Outline platelets.
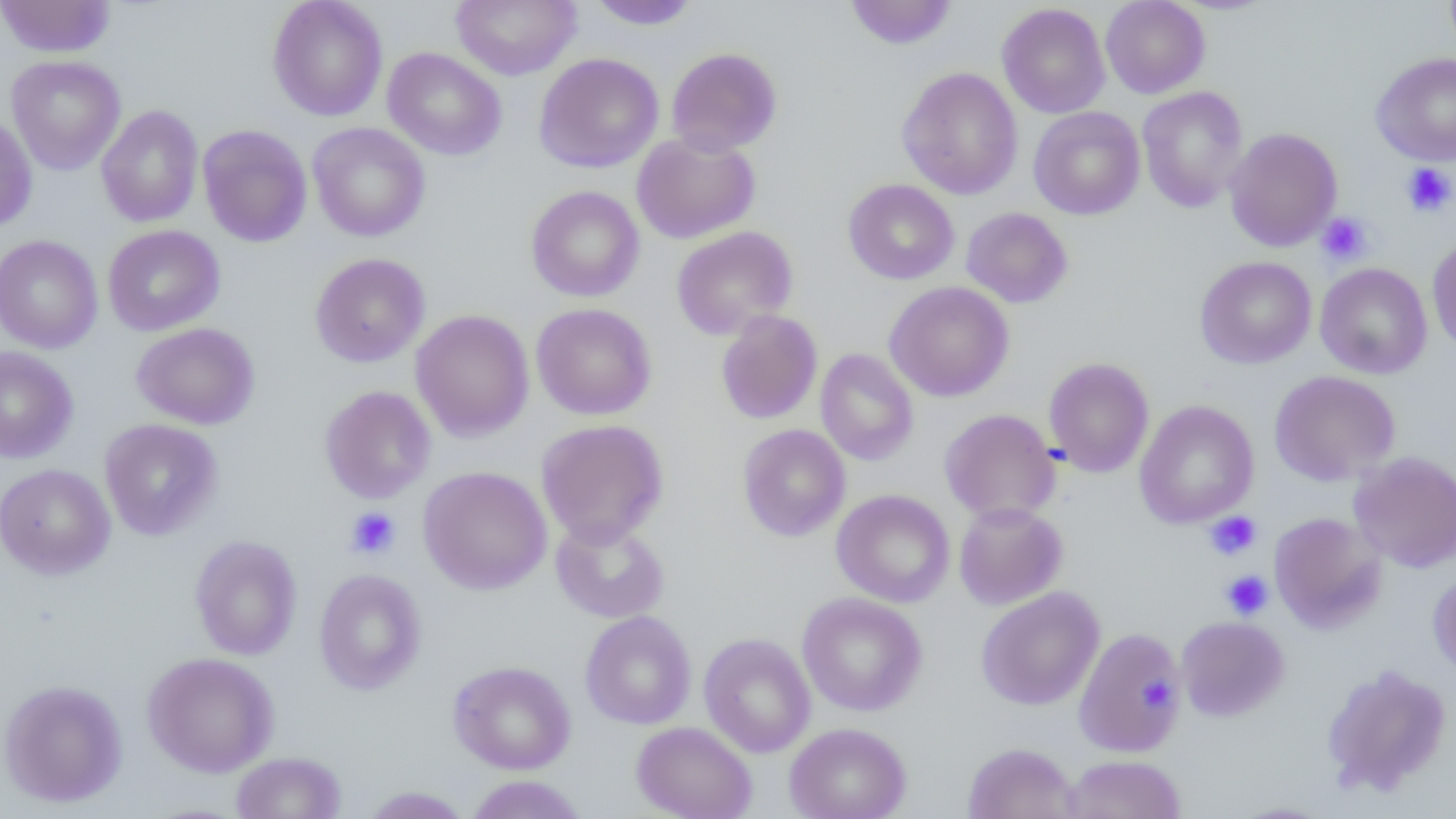

Approximate bounding boxes as (x1,y1)-(x2,y2) corner pairs in pixels.
Platelets: (1401,163)-(1455,217), (1317,212)-(1374,265), (345,507)-(401,560), (1205,511)-(1262,560), (1221,570)-(1273,620), (1141,671)-(1177,710).

slide-level diagnosis = no evidence of blood parasites
preparation = thin blood film
modality = light microscopy
image size = 1456×819 pixels
uninfected red blood cell locations = approximate bounding boxes as (x1,y1)-(x2,y2) corner pairs in pixels: (267,0)-(388,122), (451,0)-(581,80), (585,0)-(702,30), (845,0)-(958,50), (1100,0)-(1210,99), (1444,0)-(1456,58), (0,1)-(116,58), (997,3)-(1111,119), (382,47)-(507,161), (666,47)-(782,155), (533,52)-(664,173), (1371,52)-(1456,167), (5,55)-(126,175), (897,67)-(1023,200), (1136,85)-(1249,213), (96,104)-(204,227), (1028,106)-(1145,220), (0,111)-(37,232), (307,122)-(431,242), (197,124)-(312,248), (1224,127)-(1343,252), (631,132)-(760,244), (843,179)-(959,285), (526,185)-(645,302), (961,207)-(1073,308), (102,225)-(225,337), (671,225)-(798,341), (0,234)-(103,354), (1427,235)-(1456,356), (309,252)-(431,368), (1195,255)-(1317,369), (1315,262)-(1432,379), (884,281)-(1014,402), (531,302)-(657,421), (410,309)-(535,442), (715,310)-(823,424), (131,322)-(260,430), (0,346)-(79,464), (814,348)-(919,466), (1043,357)-(1155,478), (1269,370)-(1400,486), (319,385)-(436,504), (1134,399)-(1260,528), (939,408)-(1061,524), (99,419)-(223,541), (535,419)-(669,546), (737,424)-(851,541), (1349,451)-(1456,573), (0,463)-(115,580), (418,465)-(553,595), (831,489)-(955,607), (953,502)-(1067,610), (1269,512)-(1386,633), (550,516)-(670,623), (189,534)-(303,661), (314,568)-(428,695), (1428,569)-(1456,678), (976,586)-(1105,711), (797,592)-(928,717), (580,611)-(697,730), (1176,616)-(1289,721), (1073,627)-(1185,756), (699,633)-(816,757), (142,652)-(280,777), (448,660)-(576,774), (1321,663)-(1452,798), (0,679)-(128,807), (632,721)-(758,819), (784,722)-(911,819), (962,742)-(1081,819), (232,751)-(346,819), (1063,754)-(1186,819), (465,775)-(588,818), (359,786)-(473,818), (1228,801)-(1337,818)
field of view = single
magnification = 1000x